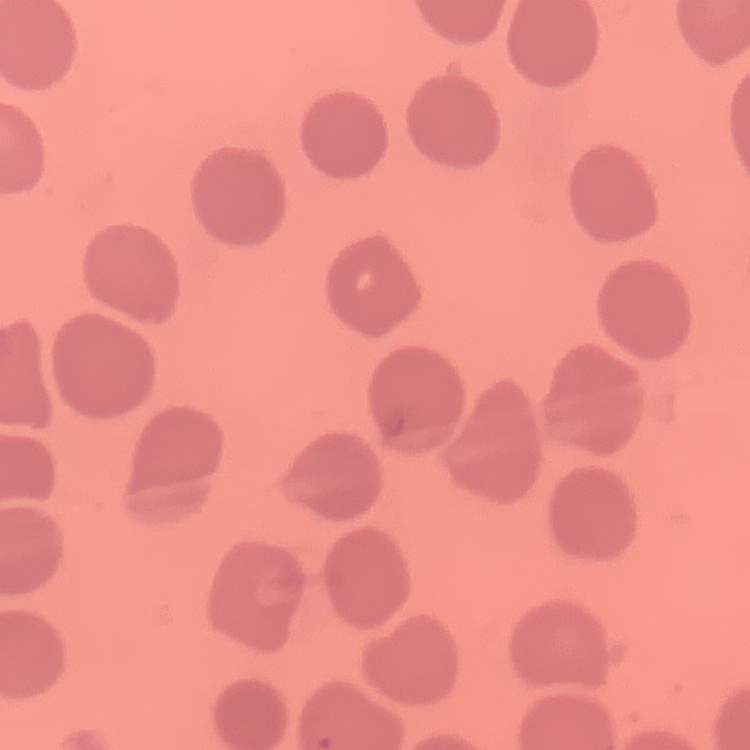 The red blood cells exhibit no rouleaux formation. Field's or Giemsa stain. Thin peripheral smear. Square crop of a larger photomicrograph.